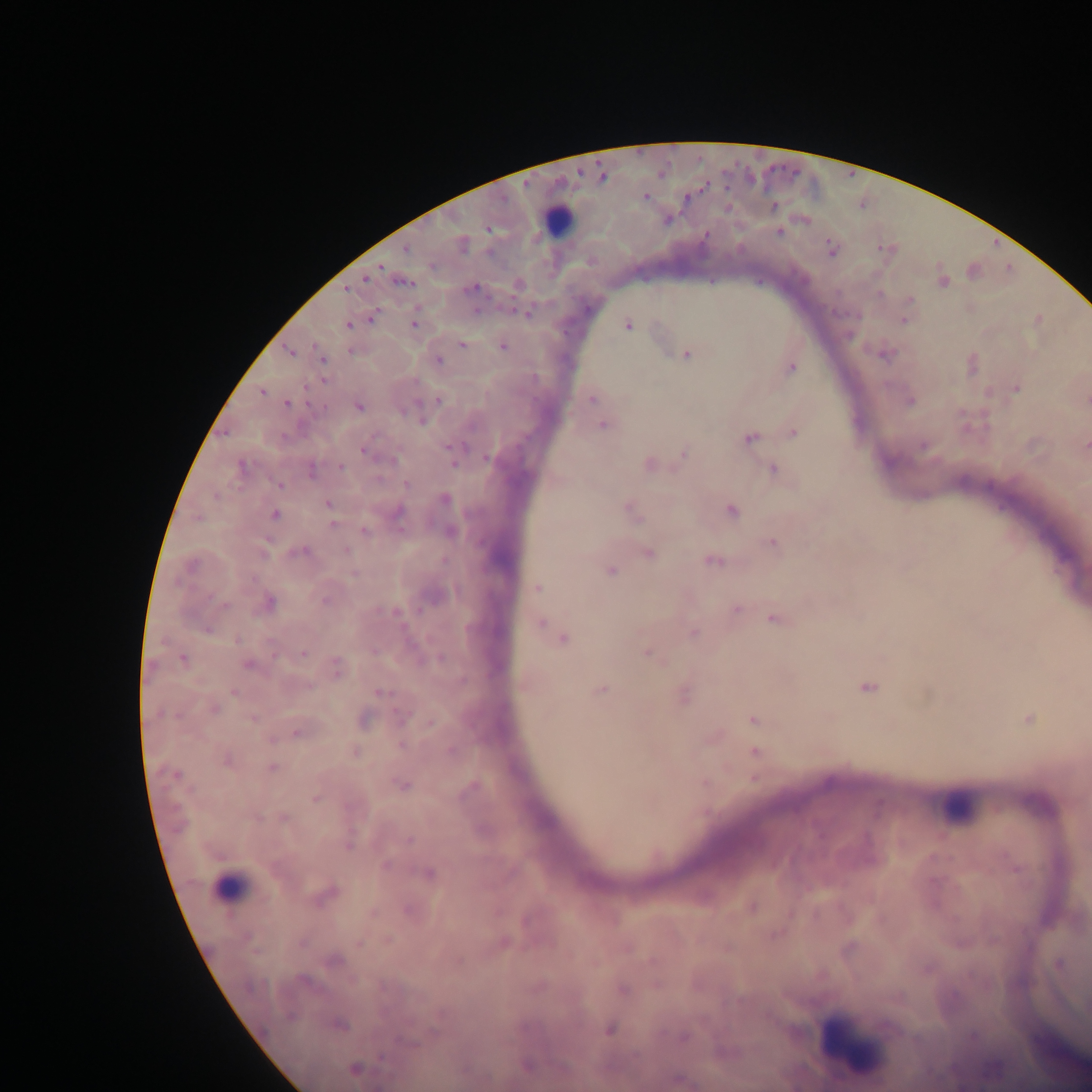
image size = 1092×1092 pixels
preparation = thick blood smear
field of view = single
capture = mobile-phone photograph through a microscope
leukocyte locations = approximate centers as x y in pixels: 555 221; 961 808; 227 885; 845 1045
malaria parasite locations = approximate centers as x y in pixels: 645 197; 487 230; 405 250; 491 252; 382 267; 365 278; 474 287; 345 291; 477 310; 512 311; 529 314; 373 315; 349 324; 414 325; 628 325; 461 345; 502 346; 686 354; 441 360; 793 367; 263 392; 592 399; 440 400; 288 403; 420 420; 602 427; 794 432; 749 440; 446 447; 364 450; 485 459; 452 464; 342 467; 772 468; 406 484; 279 485; 328 504; 730 510; 274 515; 334 524; 400 529; 364 530; 771 544; 346 550; 712 561; 611 570; 536 588; 737 609; 395 612; 774 620; 540 623; 693 633; 302 652; 647 653; 182 659; 867 688; 601 689; 379 693; 215 709; 1028 718; 752 719; 429 724; 295 730; 754 752; 273 768; 754 779; 400 785; 315 799; 283 816; 259 817; 358 944; 459 963; 1058 963; 608 1031; 381 1058
country = Ghana